Assess this cell for malaria.
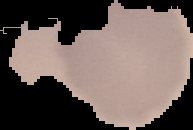
Uninfected.

Segmented cell region on a black background. From a thin blood smear. Image is 193×130 pixels.